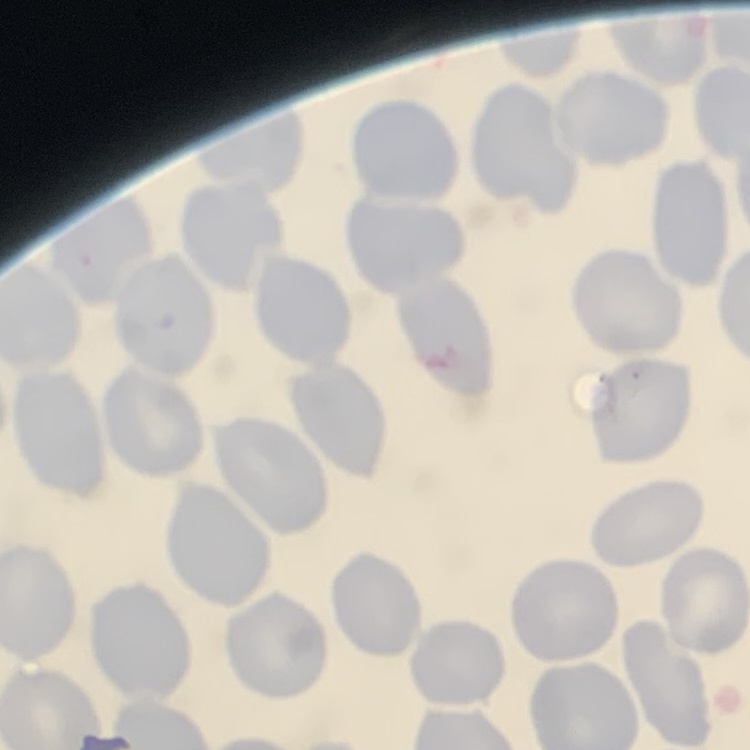
erythrocyte_morphology: no rouleaux formation
preparation: thin peripheral smear
image_type: square crop of a larger photomicrograph
stain: Field's or Giemsa